Assess the morphology of the red blood cells.
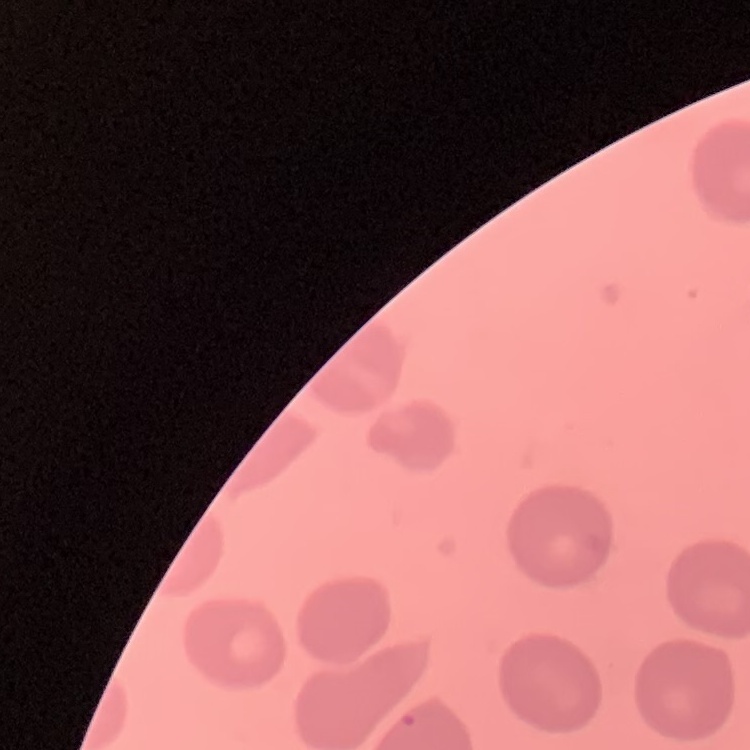

No rouleaux formation.

Stained with either Field's or Giemsa. Thin blood film. Square crop of a larger photomicrograph.